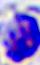

identification: leukocyte
modality: micrograph
magnification: 400x